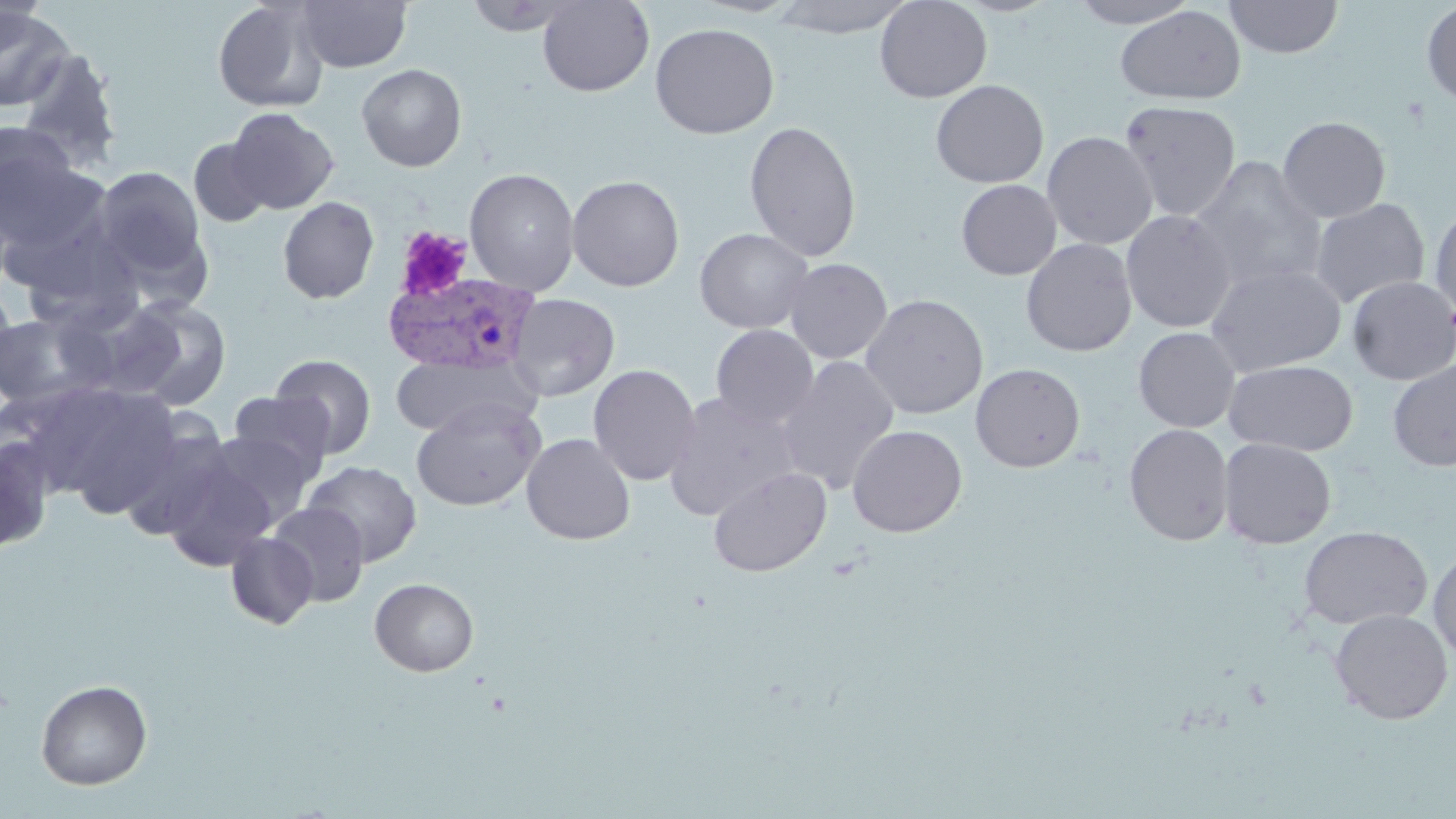

slide-level diagnosis = Plasmodium vivax
uninfected red blood cell locations = approximate bounding boxes as (x1,y1)-(x2,y2) corner pairs in pixels: (296,0)-(412,73), (463,0)-(580,36), (537,0)-(654,96), (769,0)-(917,38), (874,0)-(992,103), (1070,0)-(1199,28), (1224,0)-(1343,59), (212,1)-(329,113), (0,2)-(49,70), (1421,3)-(1456,106), (1114,4)-(1246,105), (0,6)-(75,111), (650,22)-(779,139), (16,49)-(124,173), (357,64)-(467,171), (930,79)-(1049,188), (1120,99)-(1241,222), (225,107)-(339,214), (1277,116)-(1391,223), (744,120)-(862,262), (0,123)-(79,222), (1042,131)-(1158,249), (188,138)-(272,227), (0,144)-(105,265), (1190,158)-(1327,294), (92,165)-(208,285), (464,168)-(580,295), (567,174)-(685,291), (956,179)-(1061,280), (277,197)-(380,304), (1310,198)-(1430,307), (1429,202)-(1456,319), (1121,209)-(1236,333), (695,228)-(813,334), (1021,238)-(1137,357), (784,258)-(892,364), (1206,263)-(1346,376), (1347,275)-(1456,385), (0,286)-(19,389), (506,293)-(620,401), (860,294)-(989,419), (116,296)-(233,410), (0,311)-(106,408), (710,324)-(819,430), (1133,327)-(1241,432), (270,354)-(377,459), (391,355)-(537,438), (774,356)-(900,494), (1224,359)-(1358,456), (1387,361)-(1456,471), (587,363)-(701,487), (971,363)-(1085,472), (54,387)-(184,518), (229,392)-(335,482), (663,392)-(802,521), (410,397)-(545,512), (116,419)-(233,541), (847,424)-(967,537), (1124,424)-(1234,546), (204,431)-(315,526), (521,433)-(636,545), (0,436)-(55,554), (1218,438)-(1336,549), (160,455)-(279,570), (302,460)-(423,567), (708,466)-(832,577), (267,502)-(369,607), (1298,525)-(1432,630), (225,531)-(319,629), (1428,546)-(1456,664), (369,578)-(479,677), (1329,609)-(1453,724), (35,679)-(152,790)
image size = 1456×819 pixels
field of view = one of a larger specimen
preparation = thin blood smear
stain = May-Grünwald-Giemsa
platelet locations = approximate bounding boxes as (x1,y1)-(x2,y2) corner pairs in pixels: (394,225)-(474,302)
modality = light microscopy
magnification = 1000x
Plasmodium vivax-infected red blood cell locations = approximate bounding boxes as (x1,y1)-(x2,y2) corner pairs in pixels: (383,271)-(541,375)